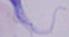

1000x magnification. A trypanosome is shown. Photomicrograph.